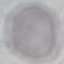

{
  "result": "no malaria parasites seen",
  "image_type": "cell patch, automatically extracted from a larger field of view and resized to 64 × 64 pixels",
  "stain": "Giemsa",
  "capture": "smartphone camera at the microscope eyepiece",
  "preparation": "thin blood smear"
}